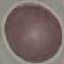
malaria status = uninfected
stain = Giemsa
preparation = thin blood film
capture = smartphone through the microscope eyepiece
image type = cell patch, automatically extracted from a larger field of view and resized to 64 × 64 pixels